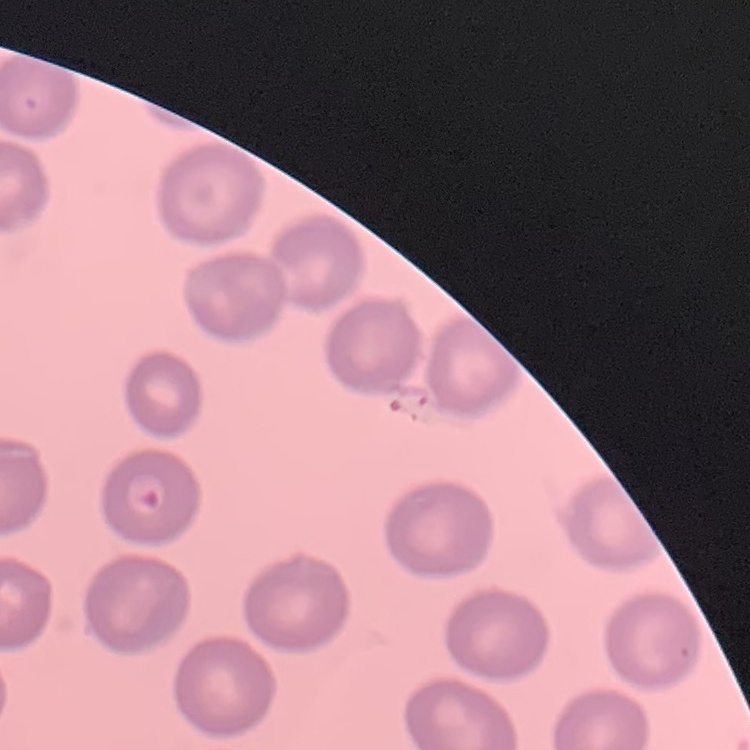

red blood cell morphology = no rouleaux formation
image type = square crop of a larger photomicrograph
stain = Field's or Giemsa
preparation = thin blood smear